Identify the cell.
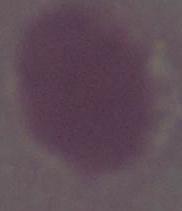

This is an erythrocyte.

magnification = 1000x
modality = micrograph